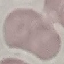

Summary:
  - Result: negative for malaria parasites
  - Preparation: thin blood smear
  - Stain: Giemsa
  - Image type: cell patch, automatically extracted from a larger field of view and resized to 64 × 64 pixels
  - Capture: smartphone through the microscope eyepiece